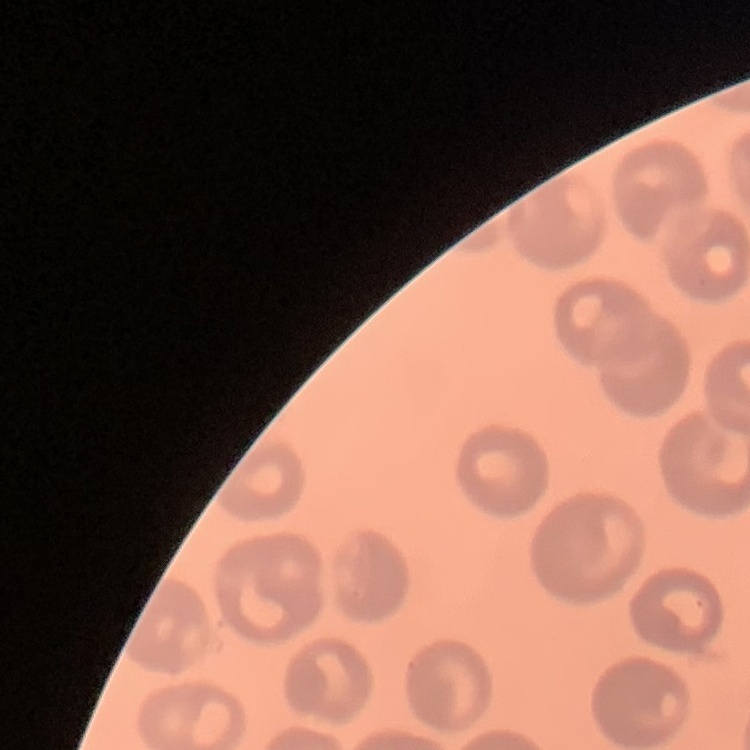
The red blood cells show no rouleaux formation. Thin blood smear. Stained with either Field's or Giemsa. One tile cut from a larger photomicrograph.